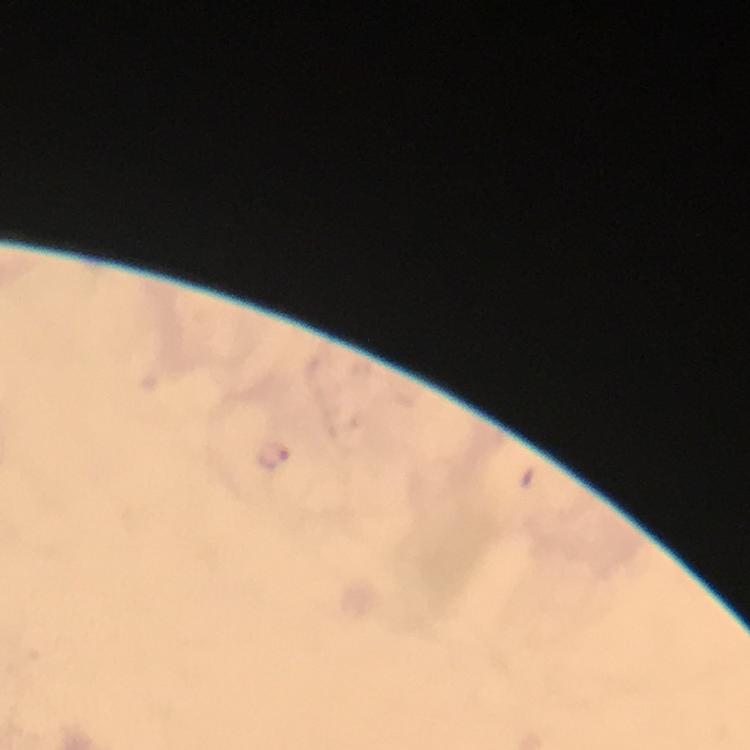 Approximate centers as (x, y) in pixels. Malaria parasite locations: (275, 460). At 100x magnification. Thick blood film. Photographed through the microscope with a smartphone camera. From a diagnostic examination for malaria. Giemsa stain. Immersion oil was used. Image is 750×750 pixels. A crop from one field of view.